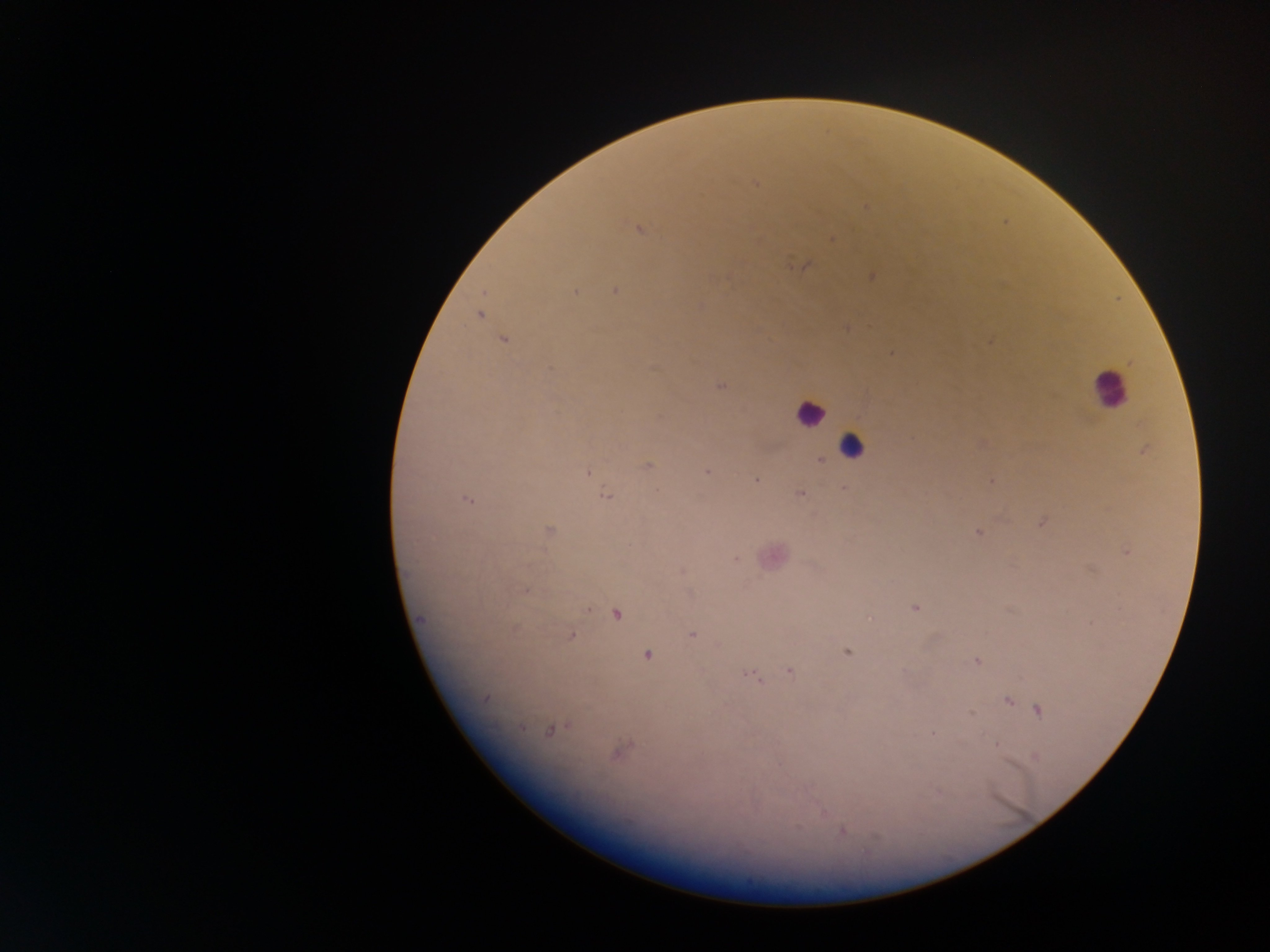

Approximate centers as x y in pixels. Leukocyte locations: 1108 389; 810 412; 851 447. Malaria parasite locations: 756 183; 865 207; 637 229; 832 238; 805 265; 871 276; 615 291; 574 293; 479 315; 847 328; 504 340; 990 342; 891 353; 719 386; 982 443; 1144 450; 821 460; 647 466; 707 472; 588 473; 756 481; 991 481; 845 488; 657 491; 800 493; 606 495; 467 500; 1041 523; 549 530; 978 532; 1127 552; 737 560; 682 572; 525 589; 916 608; 616 614; 421 619; 871 619; 692 635; 571 636; 847 651; 648 655; 978 661; 790 671; 749 674; 485 698; 1008 701; 1038 709; 971 714; 522 728; 549 730; 933 734; 996 744; 617 753; 1036 756; 939 793; 821 810; 797 827; 843 831. Sample from Ghana. Single field of view. Thick blood film. Photographed through a microscope with a mobile-phone camera. Image is 1270×952 pixels.